Comment on the morphology of the red blood cells.
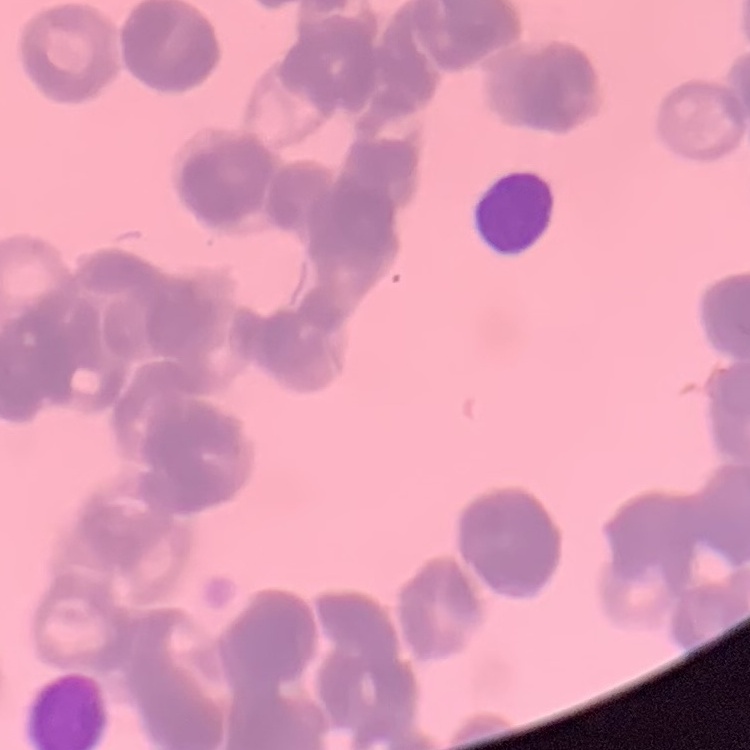
Rouleaux formation.

stain = Field's or Giemsa
preparation = thin blood film
image type = one tile cut from a larger photomicrograph